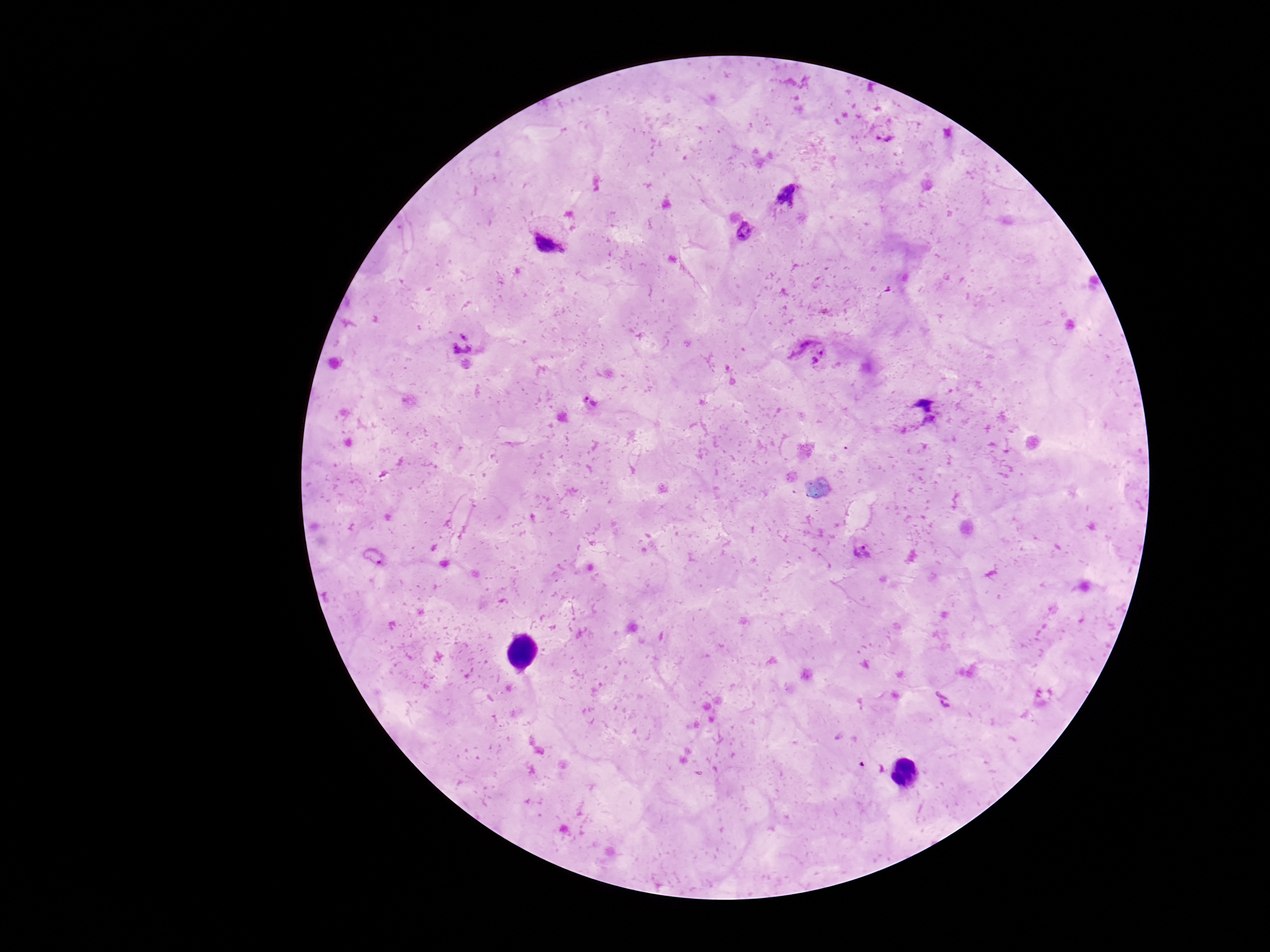
patient malaria status = positive
field of view = single
Plasmodium parasite locations = approximate object centers, in pixels from the top-left corner: (x=884, y=134), (x=789, y=193), (x=744, y=231), (x=549, y=240), (x=811, y=349), (x=464, y=352), (x=591, y=402), (x=918, y=412), (x=863, y=552), (x=943, y=699)
image size = 1270×952 pixels
preparation = thick blood smear
capture = smartphone camera through the microscope eyepiece
magnification = 100x
stain = Giemsa